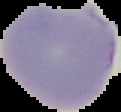

Segmented cell region on a black background. Result: malaria parasites detected. From a thin blood film. Image is 121×112 pixels.